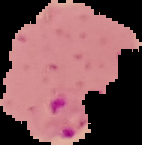
preparation: thin blood film
image_size: 142×145 pixels
result: malaria parasites detected
image_type: cell region segmented out of the field of view; surrounding area masked to black